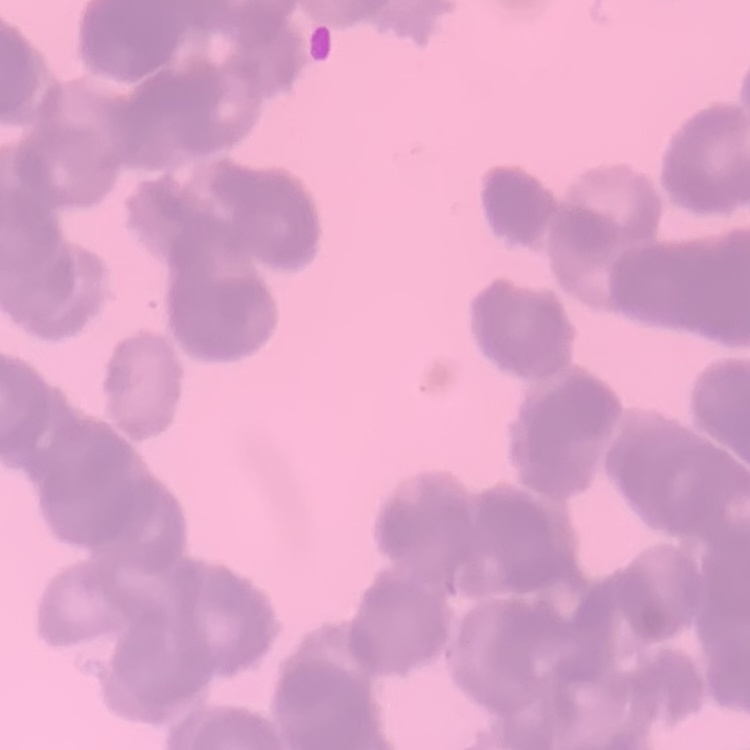

The erythrocytes show rouleaux formation. Field's or Giemsa stain. Thin blood smear. One tile cut from a larger photomicrograph.